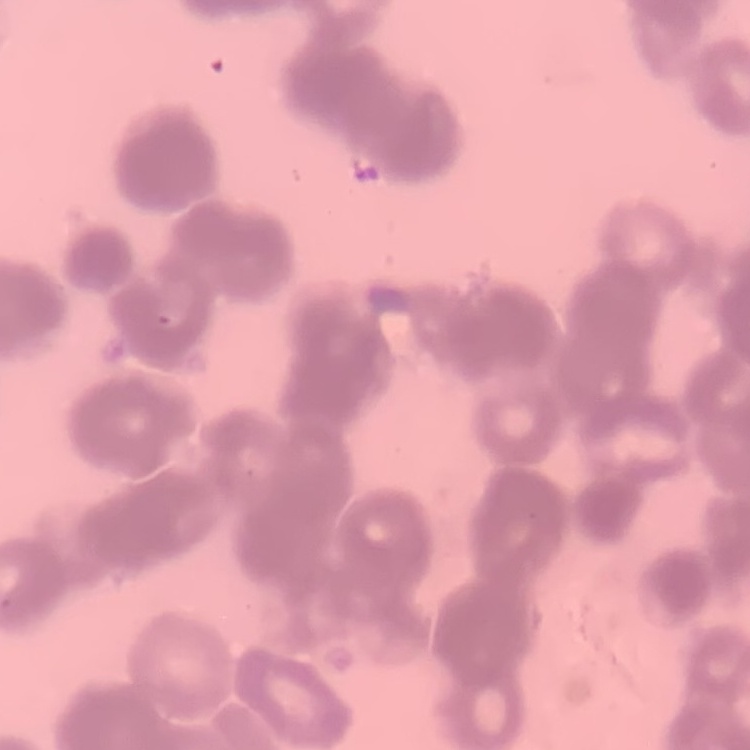

The erythrocytes exhibit rouleaux formation. Thin blood film. Square crop of a larger photomicrograph. Stained with either Field's or Giemsa.